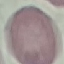
Summary:
  - Result: no malaria parasites detected
  - Capture: smartphone camera at the microscope eyepiece
  - Image type: cell patch, automatically extracted from a larger field of view and resized to 64 × 64 pixels
  - Preparation: thin blood film
  - Stain: Giemsa